Name the parasite shown.
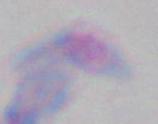

Toxoplasma gondii.

Micrograph. Captured at 1000x magnification.